Identify the blood parasite species.
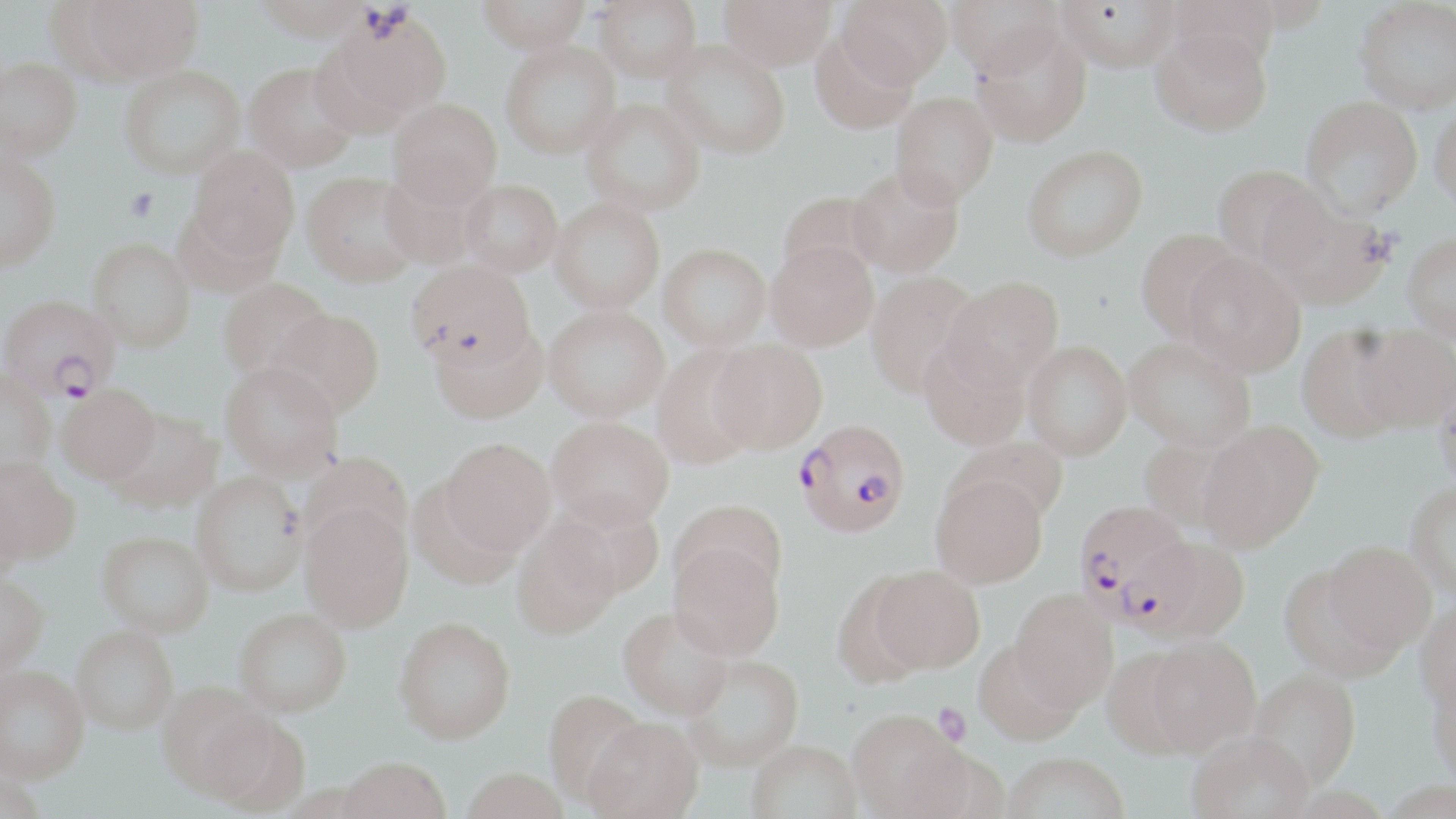

Plasmodium falciparum.

Approximate bounding boxes as (x1,y1)-(x2,y2) corner pairs in pixels. Plasmodium falciparum-infected red blood cell locations: (1,293)-(118,398), (794,418)-(911,538), (1073,501)-(1195,627). Uninfected red blood cell locations: (80,0)-(204,81), (254,0)-(372,41), (477,0)-(590,53), (594,0)-(702,82), (718,0)-(835,69), (838,0)-(951,87), (946,0)-(1063,78), (1056,0)-(1181,71), (1354,0)-(1456,113), (329,8)-(453,119), (970,24)-(1092,146), (1151,26)-(1273,136), (810,30)-(917,134), (662,39)-(790,159), (500,40)-(621,159), (0,57)-(82,161), (244,61)-(360,172), (119,65)-(245,178), (891,91)-(999,206), (1301,95)-(1423,218), (388,97)-(502,207), (581,98)-(705,215), (1430,102)-(1456,214), (1022,144)-(1148,261), (189,145)-(299,263), (0,150)-(60,271), (1212,163)-(1328,269), (380,164)-(488,270), (847,165)-(964,277), (301,171)-(421,288), (460,178)-(563,276), (777,190)-(886,285), (1262,194)-(1390,310), (550,198)-(665,314), (1135,228)-(1245,341), (1402,232)-(1456,342), (88,238)-(195,351), (765,240)-(878,351), (659,242)-(771,349), (1183,252)-(1306,376), (405,260)-(535,368), (865,271)-(981,397), (944,276)-(1064,390), (218,277)-(332,380), (543,304)-(669,421), (266,309)-(385,418), (430,321)-(547,424), (1296,326)-(1406,442), (1352,326)-(1455,431), (918,337)-(1030,450), (1124,337)-(1255,451), (709,339)-(827,452), (1023,341)-(1132,461), (651,343)-(762,467), (220,362)-(343,480), (0,367)-(55,474), (1433,375)-(1456,493), (56,383)-(160,483), (106,408)-(222,513), (547,416)-(674,530), (1197,422)-(1324,552), (950,435)-(1068,527), (1137,436)-(1245,536), (440,437)-(555,555), (299,449)-(414,556), (0,457)-(79,565), (192,470)-(306,595), (931,472)-(1049,588), (0,474)-(29,577), (1406,481)-(1456,601), (551,496)-(665,599), (672,499)-(787,601), (300,505)-(413,632), (512,520)-(620,639), (97,530)-(214,636), (1128,535)-(1251,642), (668,541)-(784,659), (1323,541)-(1436,656), (1279,564)-(1400,681), (869,565)-(984,673), (832,571)-(932,689), (0,573)-(49,676), (1010,588)-(1118,711), (1415,599)-(1456,716), (234,606)-(352,716), (619,606)-(734,719), (394,616)-(515,743), (72,625)-(178,734), (1141,636)-(1260,757), (972,638)-(1084,746), (1101,648)-(1202,758), (680,653)-(803,771), (0,665)-(88,782), (1249,667)-(1360,791), (1427,670)-(1456,790), (156,681)-(275,800), (542,689)-(648,808), (199,706)-(309,815), (847,710)-(965,818), (581,718)-(704,818), (1188,730)-(1316,819), (746,739)-(862,819), (1003,752)-(1128,819), (337,758)-(451,819), (459,767)-(570,819). Platelet locations: (126,188)-(158,222), (932,703)-(970,745). 1000x magnification. Image is 1456×819 pixels. Thin blood film. Single field of view. May-Grünwald-Giemsa-stained preparation. Light microscopy.